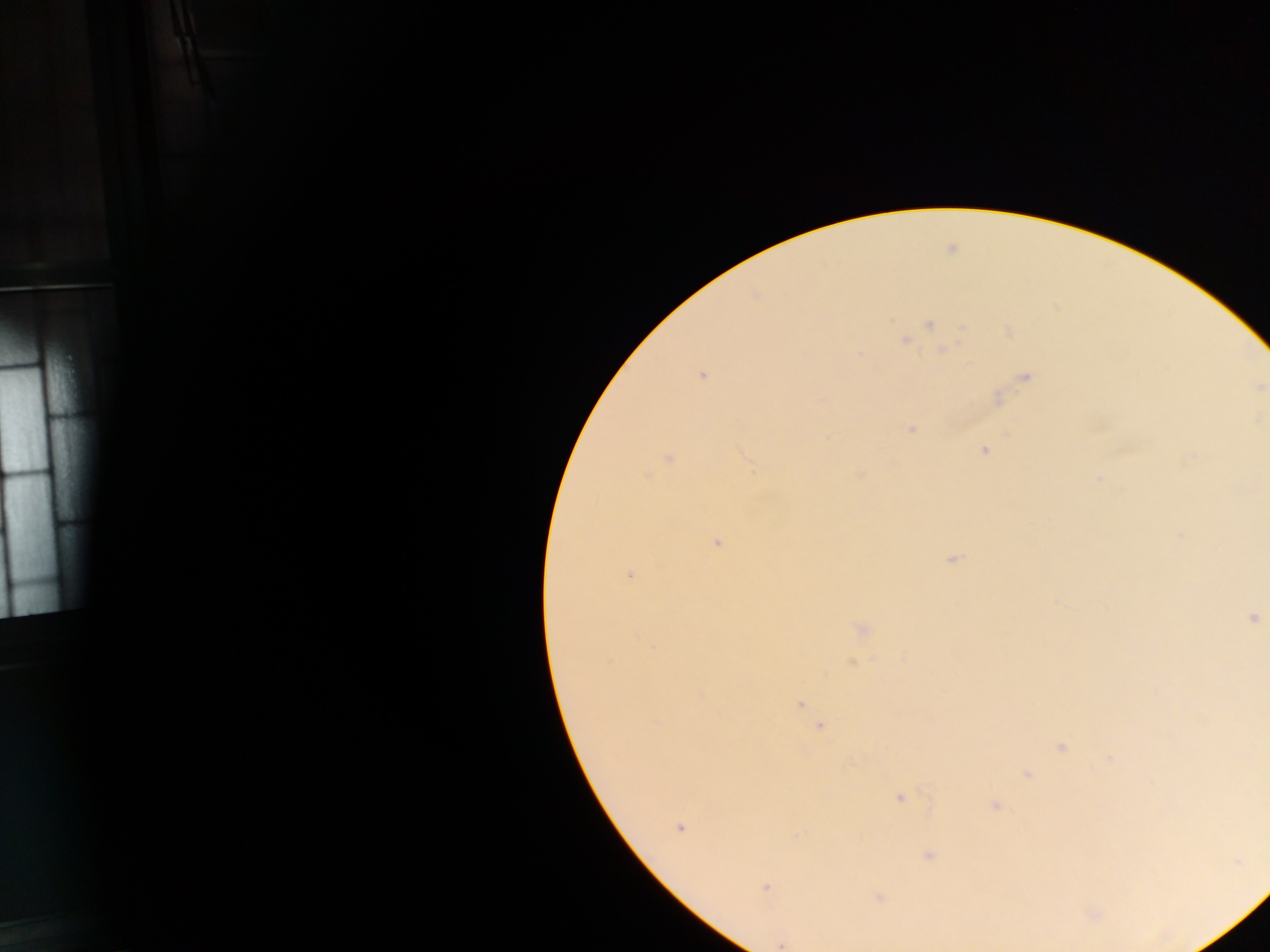 Approximate centers as x y in pixels. Malaria parasite locations: 929 324; 963 326; 1010 331; 904 340; 942 349; 859 354; 701 375; 1025 377; 911 429; 984 451; 670 459; 860 474; 646 475; 717 543; 953 558; 630 575; 1252 618; 862 629; 800 703; 821 726; 1061 746; 1027 774; 899 797; 994 805; 679 827; 928 856; 765 888; 878 897; 780 944. Single field of view. Image is 1270×952 pixels. Mobile-phone photograph taken through the microscope. Thick blood film. Sample from Ghana.